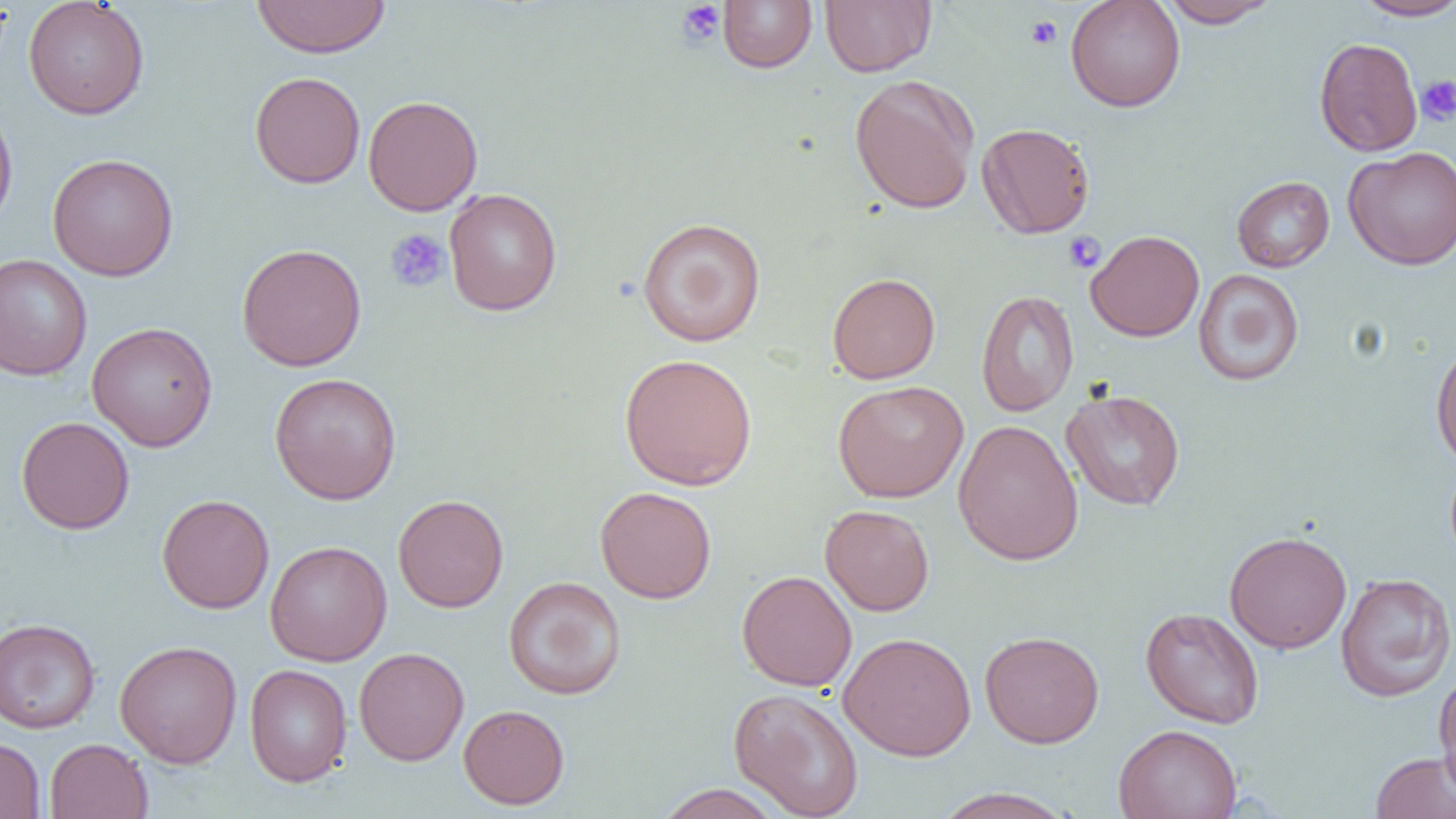

slide-level diagnosis = no evidence of blood parasites
field of view = single
modality = optical microscopy
image size = 1456×819 pixels
magnification = 1000x
platelet locations = approximate bounding boxes as named x1/y1/x2/y2 corners in pixels: (x1=675, y1=2, x2=727, y2=48), (x1=1025, y1=15, x2=1062, y2=49), (x1=1416, y1=75, x2=1456, y2=126), (x1=384, y1=228, x2=451, y2=293), (x1=1062, y1=231, x2=1106, y2=273)
preparation = thin blood film
uninfected red blood cell locations = approximate bounding boxes as named x1/y1/x2/y2 corners in pixels: (x1=252, y1=0, x2=391, y2=58), (x1=718, y1=0, x2=817, y2=72), (x1=820, y1=0, x2=936, y2=77), (x1=1065, y1=0, x2=1185, y2=112), (x1=1158, y1=0, x2=1279, y2=28), (x1=1353, y1=0, x2=1456, y2=21), (x1=22, y1=1, x2=150, y2=119), (x1=1314, y1=37, x2=1423, y2=156), (x1=249, y1=71, x2=365, y2=188), (x1=849, y1=74, x2=979, y2=215), (x1=362, y1=95, x2=483, y2=216), (x1=0, y1=100, x2=19, y2=237), (x1=976, y1=121, x2=1095, y2=238), (x1=1343, y1=146, x2=1456, y2=270), (x1=47, y1=153, x2=179, y2=281), (x1=1231, y1=176, x2=1334, y2=272), (x1=443, y1=188, x2=562, y2=316), (x1=637, y1=217, x2=766, y2=347), (x1=1085, y1=229, x2=1204, y2=342), (x1=236, y1=243, x2=367, y2=371), (x1=0, y1=253, x2=93, y2=380), (x1=1193, y1=269, x2=1304, y2=386), (x1=827, y1=272, x2=940, y2=384), (x1=976, y1=289, x2=1079, y2=417), (x1=87, y1=321, x2=218, y2=452), (x1=1430, y1=338, x2=1456, y2=470), (x1=619, y1=352, x2=758, y2=491), (x1=269, y1=372, x2=402, y2=505), (x1=832, y1=379, x2=969, y2=503), (x1=1061, y1=388, x2=1186, y2=511), (x1=16, y1=416, x2=135, y2=534), (x1=953, y1=420, x2=1084, y2=566), (x1=595, y1=486, x2=717, y2=604), (x1=157, y1=494, x2=275, y2=614), (x1=393, y1=494, x2=509, y2=613), (x1=820, y1=504, x2=935, y2=616), (x1=1224, y1=530, x2=1352, y2=653), (x1=265, y1=540, x2=392, y2=667), (x1=736, y1=570, x2=857, y2=691), (x1=1335, y1=572, x2=1455, y2=702), (x1=503, y1=576, x2=626, y2=700), (x1=1140, y1=607, x2=1265, y2=729), (x1=0, y1=617, x2=100, y2=733), (x1=979, y1=630, x2=1105, y2=748), (x1=838, y1=631, x2=977, y2=761), (x1=114, y1=640, x2=242, y2=767), (x1=354, y1=647, x2=469, y2=766), (x1=244, y1=664, x2=352, y2=787), (x1=1434, y1=670, x2=1456, y2=794), (x1=728, y1=687, x2=865, y2=819), (x1=458, y1=704, x2=570, y2=809), (x1=1113, y1=724, x2=1242, y2=819), (x1=0, y1=737, x2=45, y2=818), (x1=44, y1=738, x2=153, y2=819), (x1=1370, y1=751, x2=1456, y2=819), (x1=654, y1=784, x2=784, y2=818), (x1=931, y1=787, x2=1078, y2=819)